State the blood parasite species.
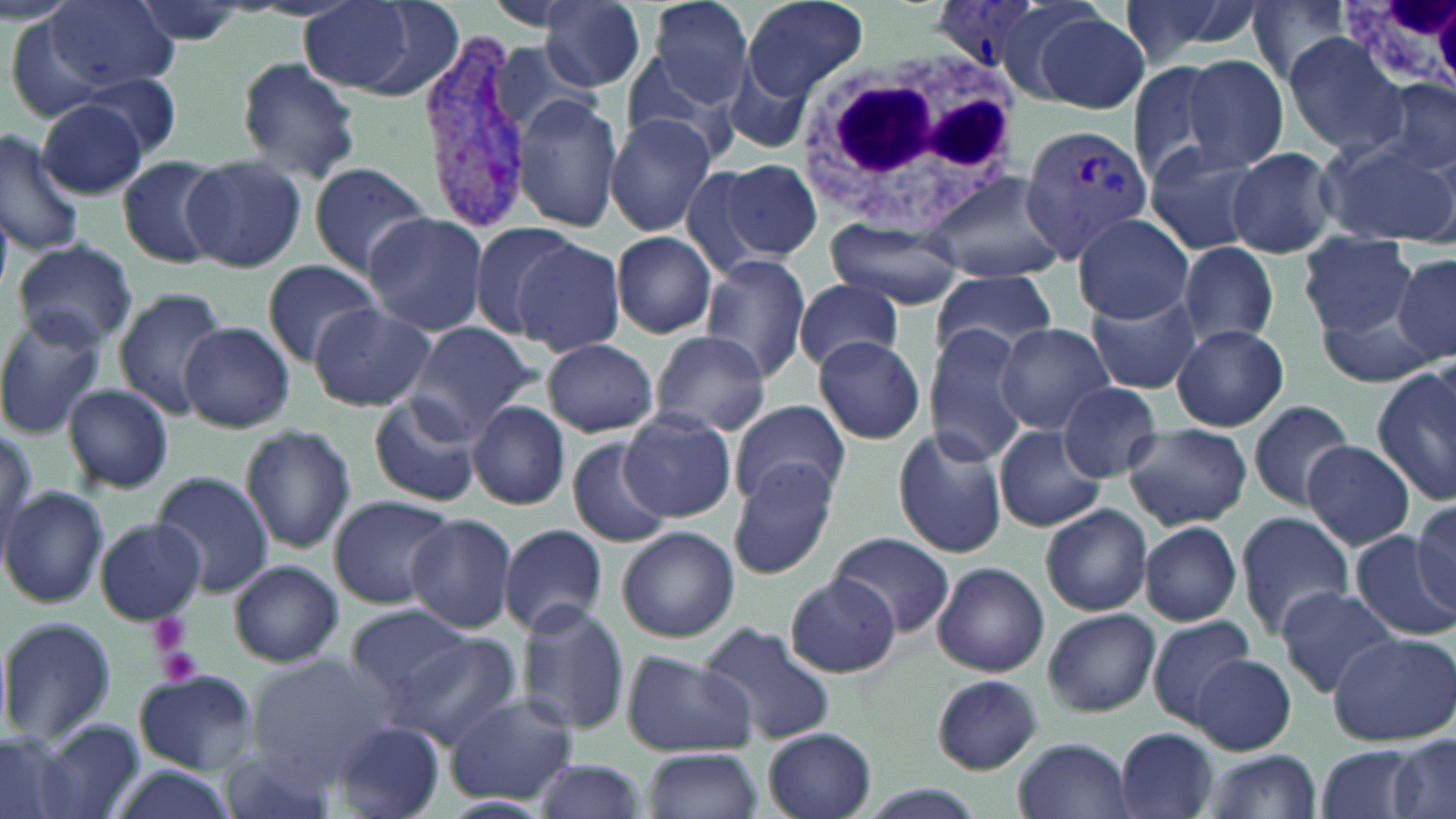

Plasmodium vivax.

Approximate bounding boxes as [x1, y1, x2, y2] in pixels. Platelet locations: [145, 612, 193, 657], [155, 645, 206, 688]. Uninfected red blood cell locations: [47, 0, 178, 89], [541, 0, 646, 90], [643, 0, 759, 108], [739, 0, 869, 100], [1114, 0, 1261, 68], [1249, 0, 1354, 87], [129, 1, 257, 46], [298, 2, 454, 99], [484, 2, 586, 32], [1033, 11, 1152, 116], [2, 14, 111, 124], [1283, 34, 1406, 156], [489, 42, 598, 142], [723, 52, 818, 159], [623, 54, 739, 162], [234, 55, 362, 185], [1182, 55, 1290, 172], [1125, 60, 1229, 187], [80, 74, 183, 158], [1375, 78, 1455, 180], [512, 96, 625, 233], [36, 99, 149, 199], [605, 112, 718, 237], [0, 130, 83, 256], [1319, 137, 1456, 245], [1143, 144, 1269, 257], [1226, 146, 1339, 258], [182, 155, 305, 273], [116, 156, 224, 268], [717, 158, 822, 265], [307, 160, 432, 279], [677, 161, 779, 282], [919, 171, 1068, 284], [363, 211, 489, 336], [1073, 212, 1195, 322], [824, 220, 966, 310], [465, 223, 593, 341], [611, 232, 719, 340], [1301, 234, 1417, 339], [11, 238, 138, 350], [513, 239, 627, 355], [1177, 242, 1279, 348], [1391, 254, 1456, 365], [699, 255, 812, 380], [262, 259, 381, 364], [931, 270, 1060, 364], [793, 277, 906, 373], [112, 288, 227, 418], [1087, 290, 1201, 395], [307, 304, 436, 412], [1315, 304, 1444, 388], [0, 312, 110, 440], [993, 321, 1118, 436], [402, 322, 541, 440], [180, 323, 295, 432], [1173, 324, 1289, 431], [927, 325, 1035, 464], [648, 330, 772, 436], [813, 335, 926, 444], [543, 340, 659, 435], [1374, 367, 1456, 503], [62, 382, 175, 493], [1058, 382, 1163, 480], [368, 394, 481, 507], [1246, 398, 1356, 510], [467, 400, 571, 509], [731, 400, 851, 508], [621, 410, 736, 521], [1124, 422, 1252, 529], [240, 424, 357, 553], [893, 426, 1010, 560], [994, 427, 1106, 533], [565, 436, 673, 550], [1304, 440, 1416, 551], [277, 461, 416, 591], [728, 463, 842, 580], [150, 471, 272, 595], [0, 486, 108, 609], [328, 494, 455, 609], [1412, 500, 1455, 609], [1039, 503, 1153, 617], [1236, 511, 1354, 640], [405, 514, 517, 632], [93, 517, 206, 623], [499, 522, 609, 638], [1138, 522, 1242, 625], [616, 525, 740, 643], [1350, 531, 1456, 638], [833, 533, 953, 637], [229, 560, 342, 667], [932, 562, 1050, 677], [785, 575, 902, 678], [1276, 586, 1398, 696], [513, 600, 630, 738], [348, 604, 473, 699], [1042, 608, 1160, 716], [1147, 615, 1258, 725], [0, 616, 116, 747], [697, 622, 838, 747], [1328, 633, 1454, 746], [388, 634, 522, 750], [619, 649, 758, 757], [1192, 654, 1295, 753], [245, 656, 395, 776], [134, 672, 257, 773], [930, 675, 1043, 773], [443, 694, 579, 806], [32, 721, 146, 819], [330, 722, 447, 818], [1115, 727, 1219, 819], [763, 728, 878, 819], [0, 733, 79, 819], [1389, 735, 1454, 819], [1012, 737, 1138, 819], [218, 743, 348, 819], [1312, 744, 1425, 819], [642, 748, 762, 819], [1206, 752, 1322, 819], [532, 757, 649, 819], [105, 764, 241, 819], [852, 786, 991, 819], [437, 794, 557, 819]. Plasmodium vivax-infected red blood cell locations: [931, 1, 1052, 80], [418, 38, 540, 230], [1018, 120, 1154, 261]. White blood cell locations: [1344, 0, 1456, 104], [790, 49, 1024, 236]. Captured at 1000x magnification. Thin blood smear. Single field of view. Light microscopy. May-Grünwald-Giemsa-stained preparation. Image is 1456×819 pixels.